Assess the morphology of the red blood cells.
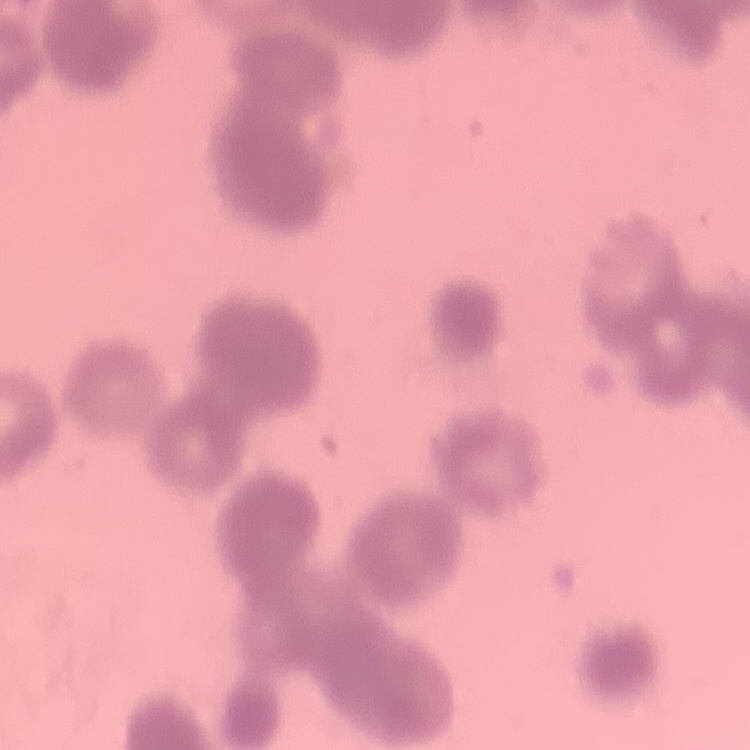

They show rouleaux formation.

Thin peripheral smear. Square crop of a larger photomicrograph. Stained with either Field's or Giemsa.